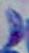

identification = Toxoplasma gondii
modality = photomicrograph
magnification = 1000x